Report the malaria status of this cell.
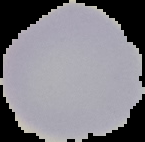
Uninfected.

{
  "image_type": "segmented cell region on a black background",
  "image_size": "145×142 pixels",
  "preparation": "thin blood film"
}